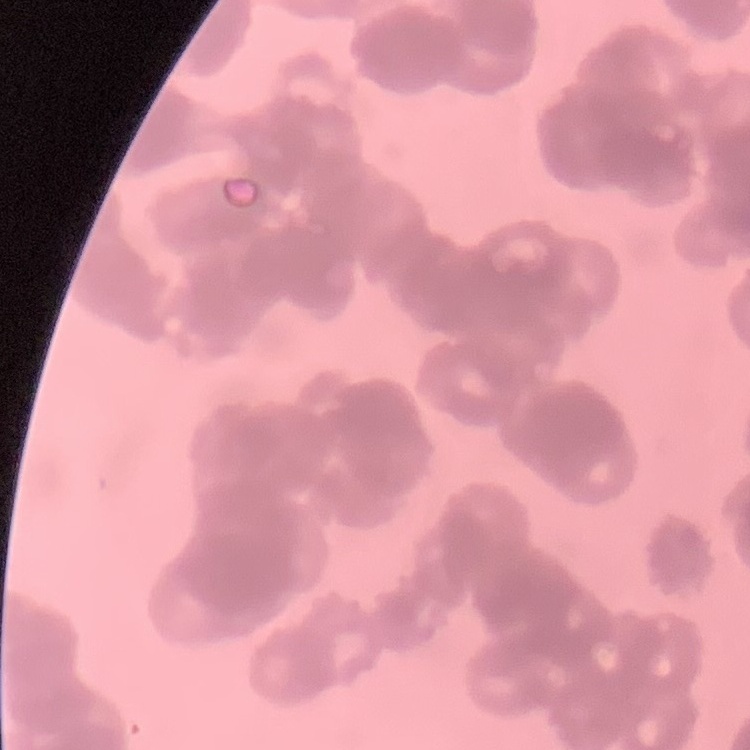
The red blood cells exhibit rouleaux formation. One tile cut from a larger photomicrograph. Thin peripheral smear. Field's or Giemsa stain.